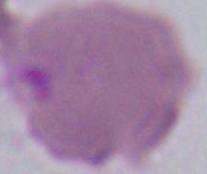
Summary:
  - Modality: photomicrograph
  - Identification: erythrocyte
  - Magnification: 1000x